Describe the morphology of the erythrocytes.
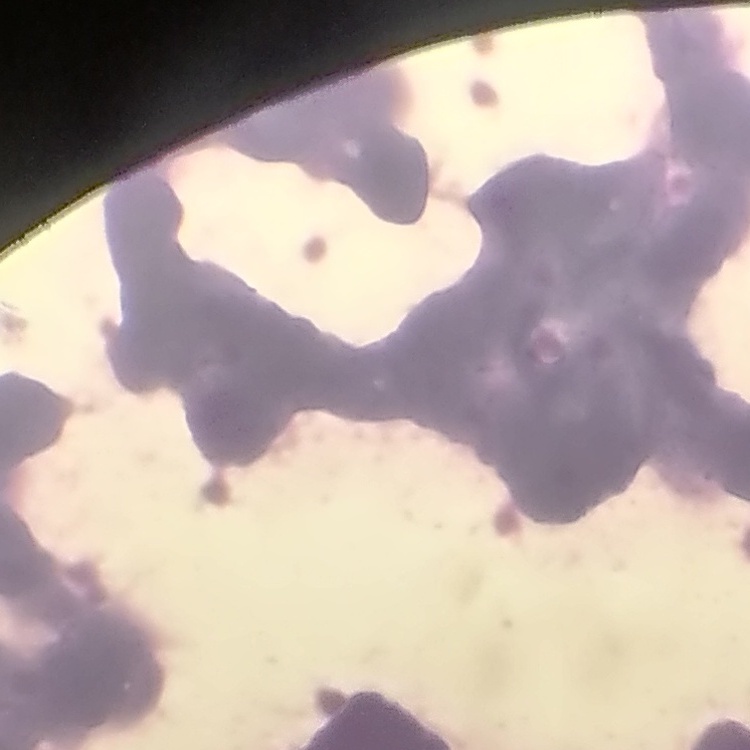

They show rouleaux formation.

preparation: thin blood film
image_type: square crop of a larger photomicrograph
stain: Field's or Giemsa